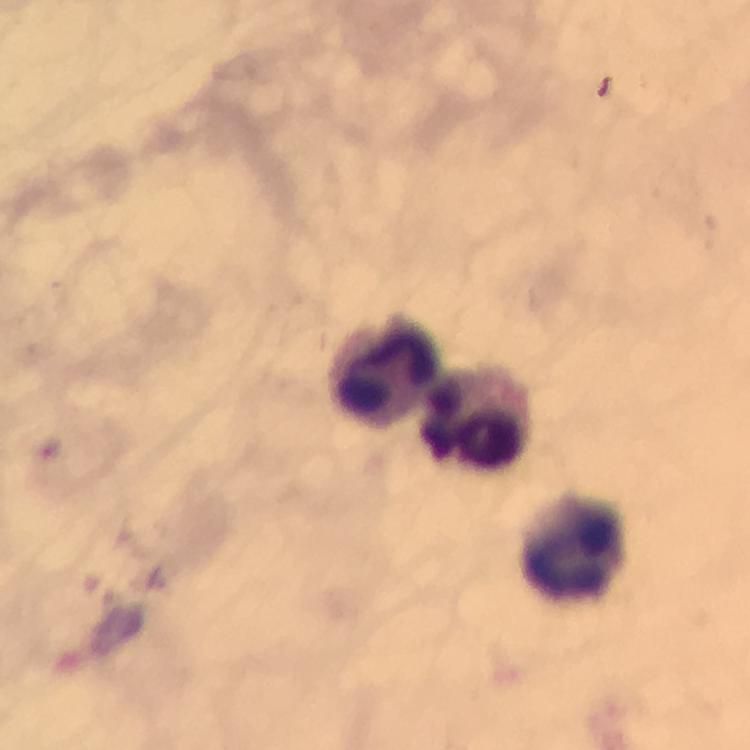

{
  "preparation": "thick smear",
  "capture": "smartphone mounted on the microscope",
  "leukocyte_locations": "approximate object centers, in pixels from the top-left corner: (x=383, y=367), (x=477, y=416), (x=569, y=546)",
  "cropped_from": "one field of view",
  "stain": "Giemsa",
  "plasmodium_parasites": "none detected",
  "immersion_oil": "applied",
  "context": "from a diagnostic examination for malaria",
  "image_size": "750×750 pixels",
  "magnification": "100x"
}